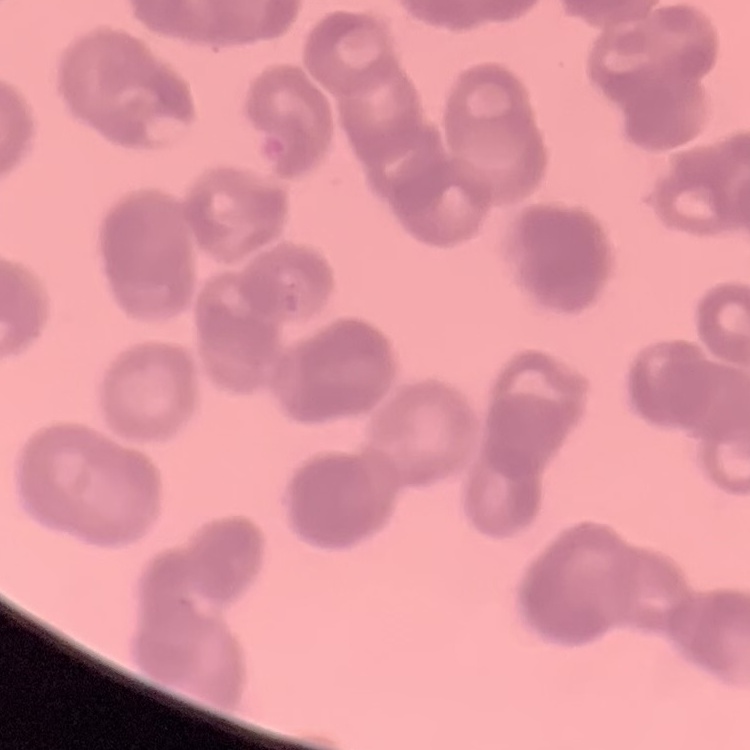

erythrocyte morphology = rouleaux formation
image type = square crop of a larger photomicrograph
preparation = thin peripheral smear
stain = Field's or Giemsa